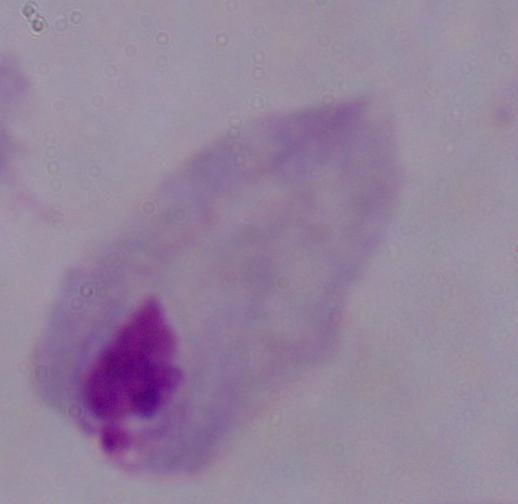
modality = micrograph
identification = trichomonad
magnification = 1000x